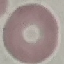
{
  "result": "no malaria parasites seen",
  "capture": "smartphone through the microscope eyepiece",
  "stain": "Giemsa",
  "preparation": "thin blood smear",
  "image_type": "automatically extracted cell patch, resized to 64 × 64 pixels"
}